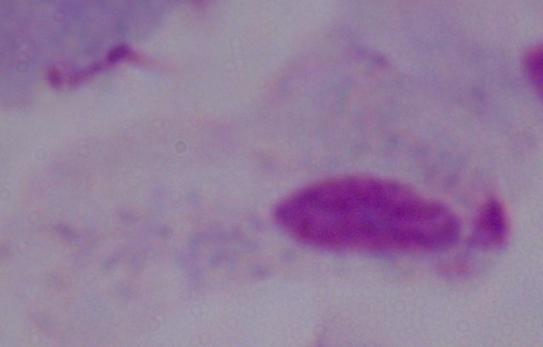

{
  "modality": "micrograph",
  "magnification": "1000x",
  "identification": "trichomonad"
}